Assess the morphology of the erythrocytes.
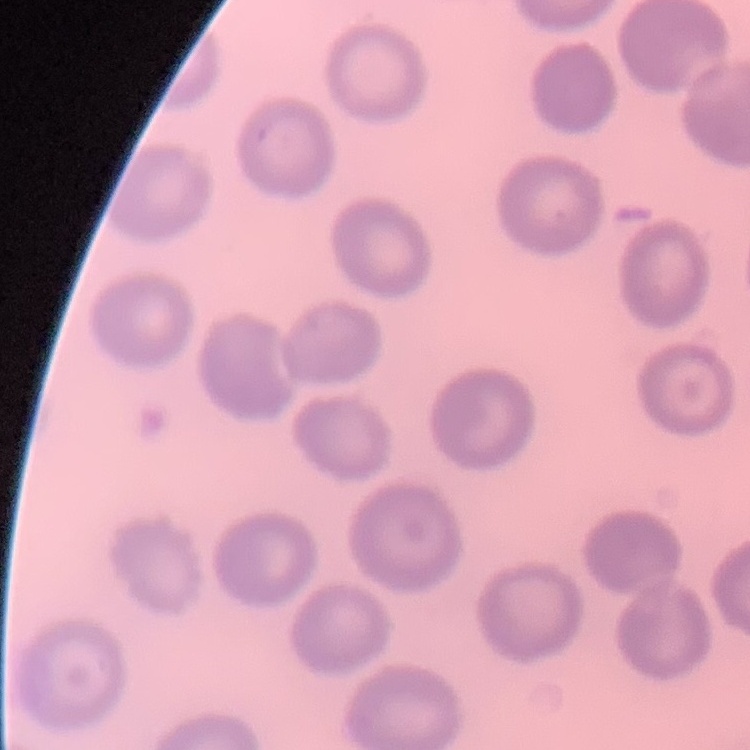

They show no rouleaux formation.

stain = Field's or Giemsa
image type = one tile cut from a larger photomicrograph
preparation = thin peripheral smear